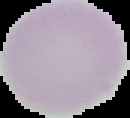
Malaria status: uninfected. From a thin blood smear. Segmented cell region on a black background. Image is 130×118 pixels.